Locate every uninfected red blood cell.
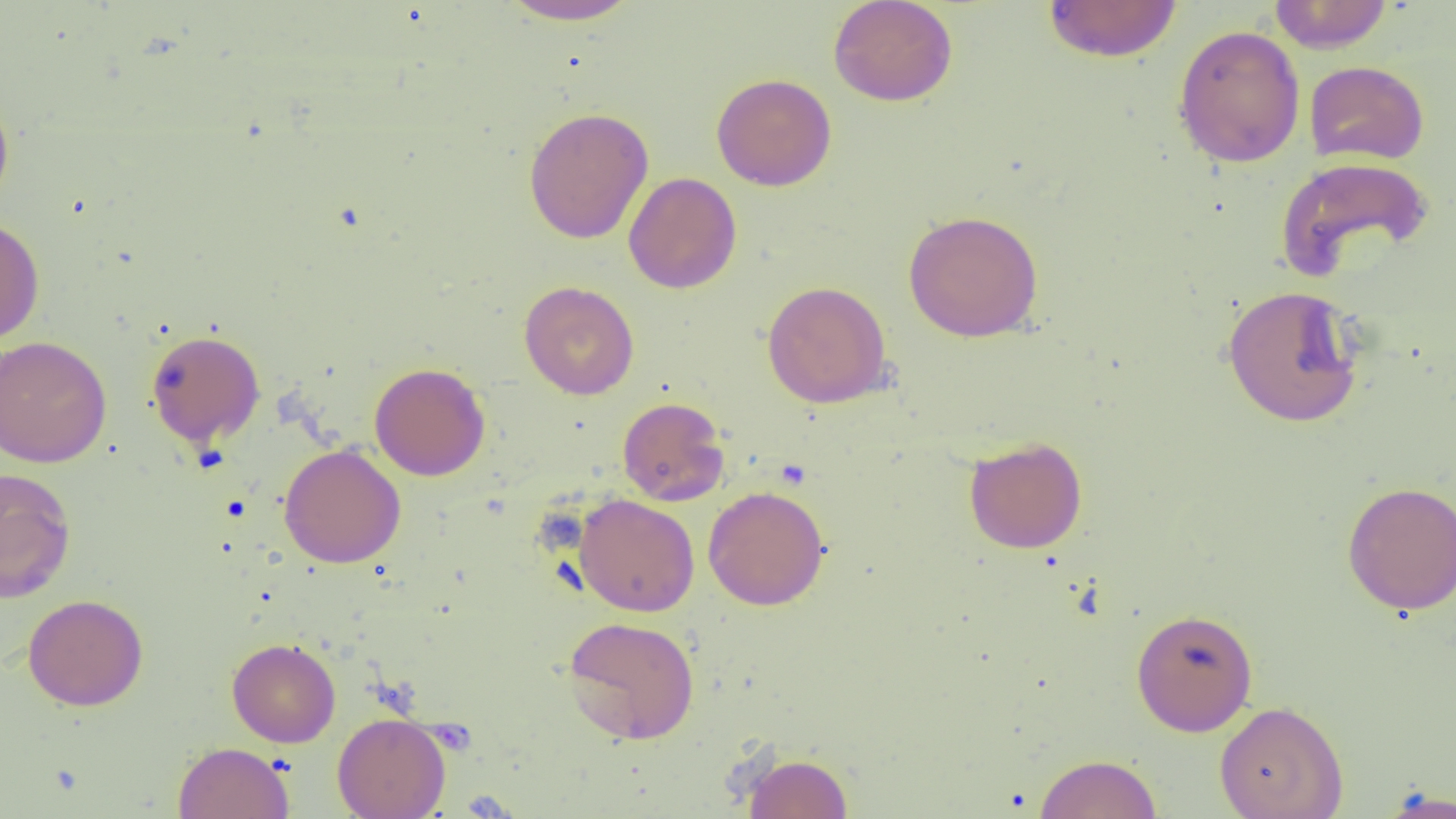
Approximate bounding boxes as named x1/y1/x2/y2 corners in pixels.
Uninfected red blood cells: (x1=498, y1=0, x2=643, y2=26), (x1=828, y1=0, x2=958, y2=106), (x1=1042, y1=1, x2=1182, y2=63), (x1=1268, y1=1, x2=1394, y2=53), (x1=1172, y1=24, x2=1306, y2=168), (x1=1304, y1=60, x2=1429, y2=165), (x1=711, y1=73, x2=837, y2=191), (x1=0, y1=91, x2=15, y2=213), (x1=523, y1=106, x2=653, y2=244), (x1=1275, y1=156, x2=1435, y2=282), (x1=623, y1=172, x2=742, y2=294), (x1=903, y1=209, x2=1043, y2=342), (x1=0, y1=215, x2=45, y2=344), (x1=519, y1=281, x2=639, y2=399), (x1=762, y1=281, x2=892, y2=408), (x1=1221, y1=284, x2=1365, y2=428), (x1=146, y1=329, x2=265, y2=447), (x1=0, y1=335, x2=112, y2=468), (x1=369, y1=362, x2=490, y2=480), (x1=617, y1=397, x2=729, y2=506), (x1=963, y1=436, x2=1088, y2=553), (x1=279, y1=444, x2=406, y2=568), (x1=0, y1=466, x2=77, y2=603), (x1=1341, y1=480, x2=1456, y2=616), (x1=703, y1=485, x2=829, y2=611), (x1=573, y1=493, x2=700, y2=617), (x1=23, y1=594, x2=149, y2=711), (x1=1130, y1=607, x2=1258, y2=736), (x1=562, y1=615, x2=700, y2=744), (x1=227, y1=637, x2=341, y2=747), (x1=1214, y1=701, x2=1348, y2=819), (x1=332, y1=712, x2=451, y2=819), (x1=173, y1=741, x2=294, y2=819), (x1=743, y1=753, x2=853, y2=818), (x1=1034, y1=754, x2=1162, y2=818), (x1=1377, y1=786, x2=1456, y2=818).

slide_level_diagnosis: negative for blood parasites
preparation: thin blood smear
field_of_view: one of a larger specimen
magnification: 1000x
modality: optical microscopy
image_size: 1456×819 pixels